Locate every malaria parasite and every leukocyte.
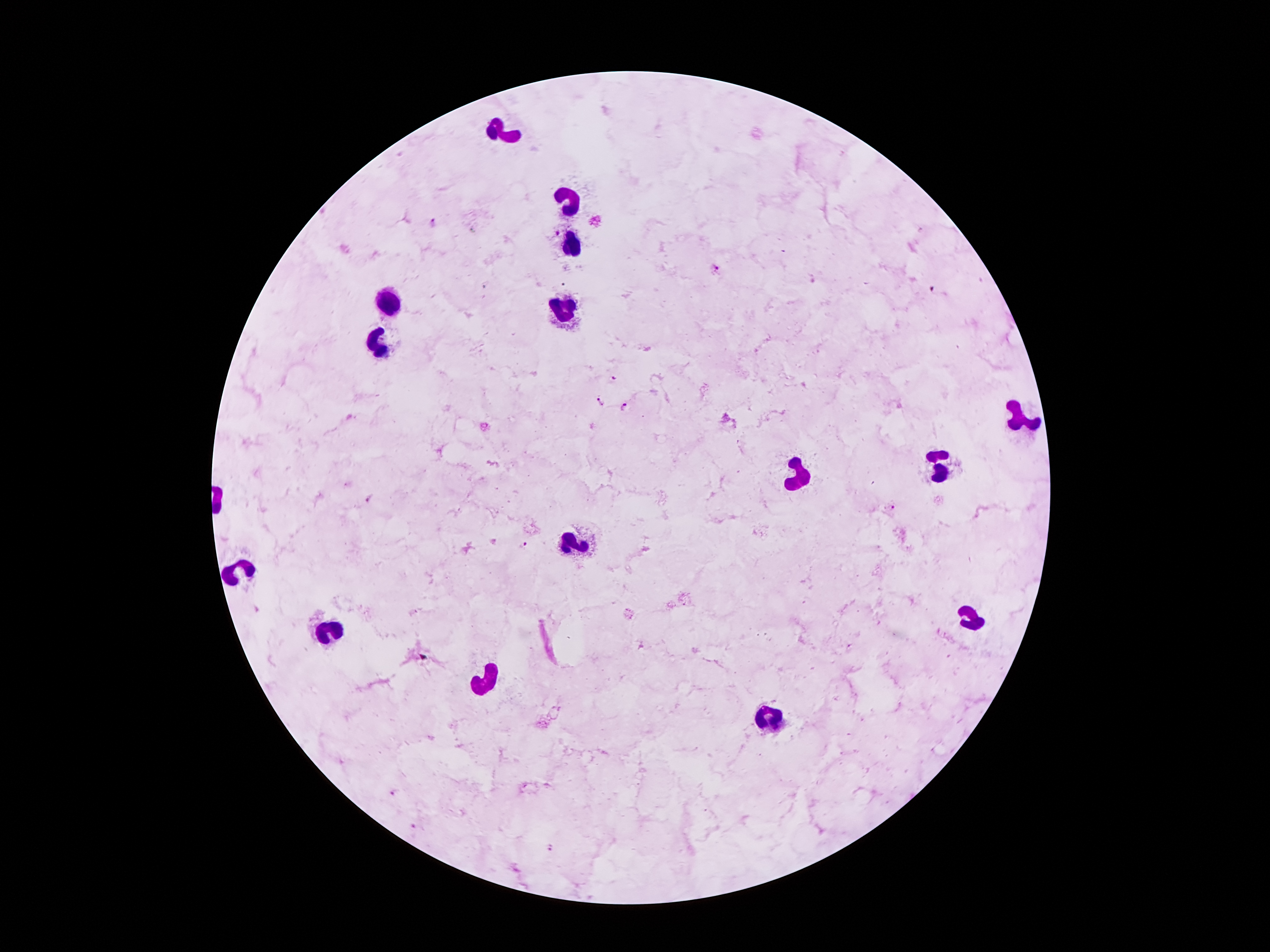

Approximate centers as {x, y} in pixels.
Malaria parasites: {433, 222}, {716, 268}, {615, 377}, {601, 402}, {625, 407}, {371, 500}, {893, 508}, {525, 546}, {392, 791}, {414, 827}, {552, 850}.
Leukocytes: {509, 131}, {566, 204}, {572, 250}, {387, 305}, {567, 312}, {379, 343}, {1014, 418}, {940, 467}, {799, 478}, {579, 541}, {241, 571}, {973, 622}, {328, 635}, {480, 679}, {772, 717}.

image size = 1270×952 pixels
preparation = thick blood smear
field of view = one from this slide
magnification = 100x
patient malaria status = infected with Plasmodium falciparum
capture = smartphone through the microscope eyepiece
stain = Giemsa